Locate every blood parasite and identify its species.
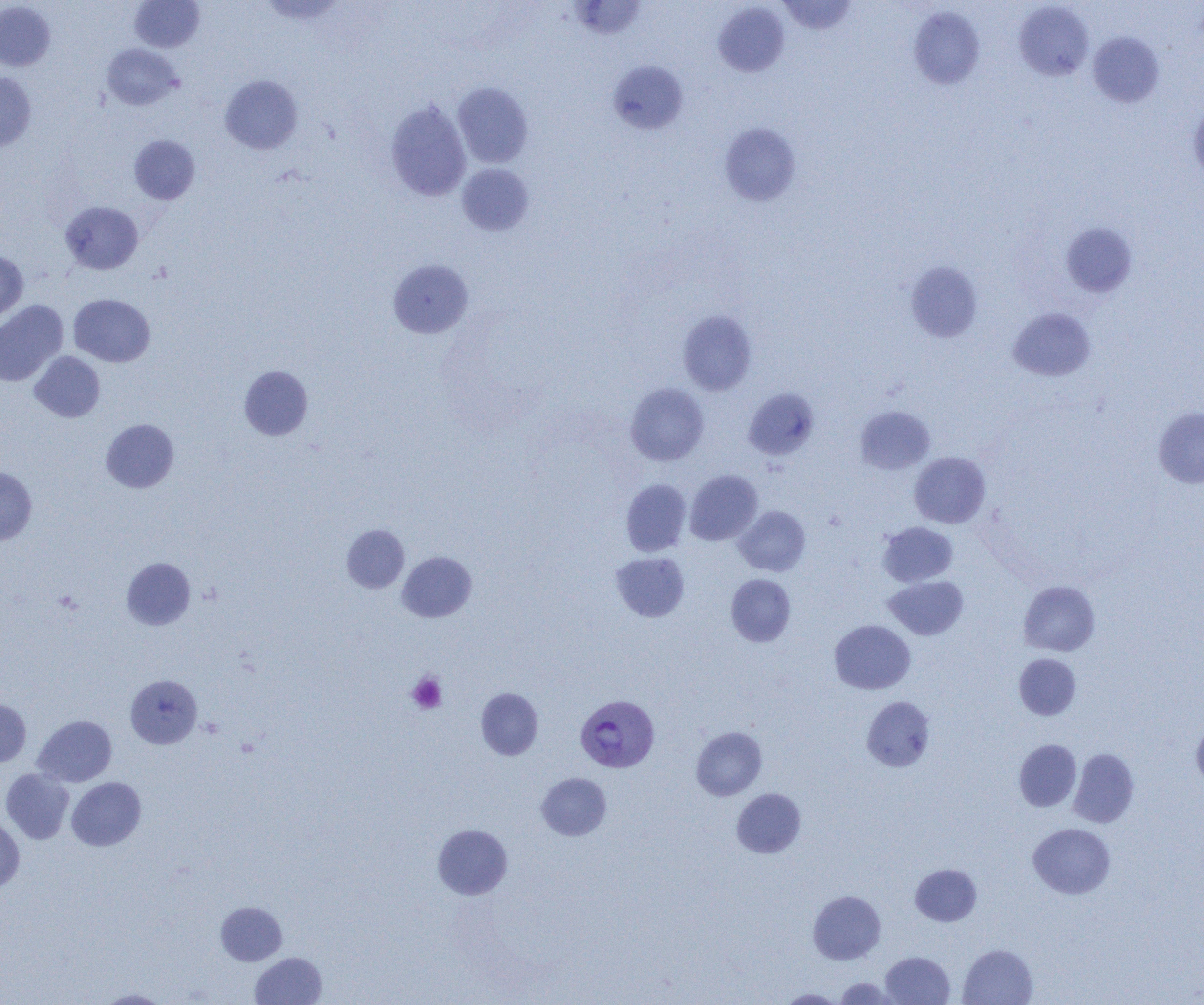

Approximate bounding boxes as (x1,y1)-(x2,y2) corner pairs in pixels.
Plasmodium vivax-infected red blood cells: (576,694)-(660,773).
No Plasmodium falciparum, Plasmodium ovale, Plasmodium malariae, Babesia divergens, or Trypanosoma brucei observed.

Summary:
  - Uninfected red blood cell locations: (130,0)-(205,53), (0,1)-(55,71), (569,1)-(647,39), (777,1)-(857,35), (1014,1)-(1094,81), (713,2)-(789,77), (908,6)-(985,89), (1087,32)-(1164,107), (101,44)-(181,110), (608,61)-(688,135), (0,71)-(36,151), (220,75)-(303,154), (452,82)-(533,167), (1187,99)-(1204,184), (386,100)-(471,201), (719,123)-(801,206), (129,135)-(200,204), (457,164)-(533,236), (60,200)-(143,274), (1060,222)-(1137,297), (0,250)-(28,321), (388,259)-(473,338), (905,261)-(983,343), (68,294)-(155,366), (0,300)-(67,386), (1008,307)-(1096,381), (678,310)-(757,395), (30,351)-(105,422), (239,365)-(313,440), (625,382)-(709,466), (743,388)-(819,460), (856,406)-(935,474), (1154,407)-(1204,488), (101,419)-(179,492), (910,452)-(990,528), (0,466)-(37,545), (685,470)-(762,545), (621,479)-(691,556), (734,506)-(811,576), (878,522)-(958,586), (341,524)-(409,593), (397,551)-(476,622), (611,552)-(689,622), (121,557)-(195,630), (726,574)-(796,646), (884,575)-(968,640), (1018,580)-(1100,656), (829,620)-(915,694), (1014,653)-(1081,720), (125,675)-(202,748), (476,688)-(543,760), (862,696)-(935,771), (0,699)-(31,766), (33,715)-(117,786), (1191,718)-(1204,792), (691,726)-(767,800), (1014,739)-(1081,811), (1068,748)-(1139,828), (1,768)-(73,844), (536,772)-(612,840), (67,777)-(146,851), (732,788)-(806,858), (0,815)-(24,893), (1028,823)-(1116,899), (433,824)-(513,899), (910,863)-(982,926), (807,890)-(885,964), (216,902)-(287,965), (957,944)-(1038,1005), (880,951)-(955,1004), (250,952)-(327,1005), (833,976)-(900,1004), (776,988)-(847,1004), (96,989)-(170,1004)
  - Platelet locations: (408,673)-(447,713)
  - Slide-level diagnosis: Plasmodium vivax
  - Modality: optical microscopy
  - Preparation: thin blood smear
  - Field of view: one of a larger specimen
  - Magnification: 1000x
  - Image size: 1204×1005 pixels